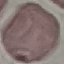
Summary:
  - Malaria status: uninfected
  - Stain: Giemsa
  - Image type: cell patch, automatically extracted from a larger field of view and resized to 64 × 64 pixels
  - Capture: smartphone camera at the microscope eyepiece
  - Preparation: thin smear